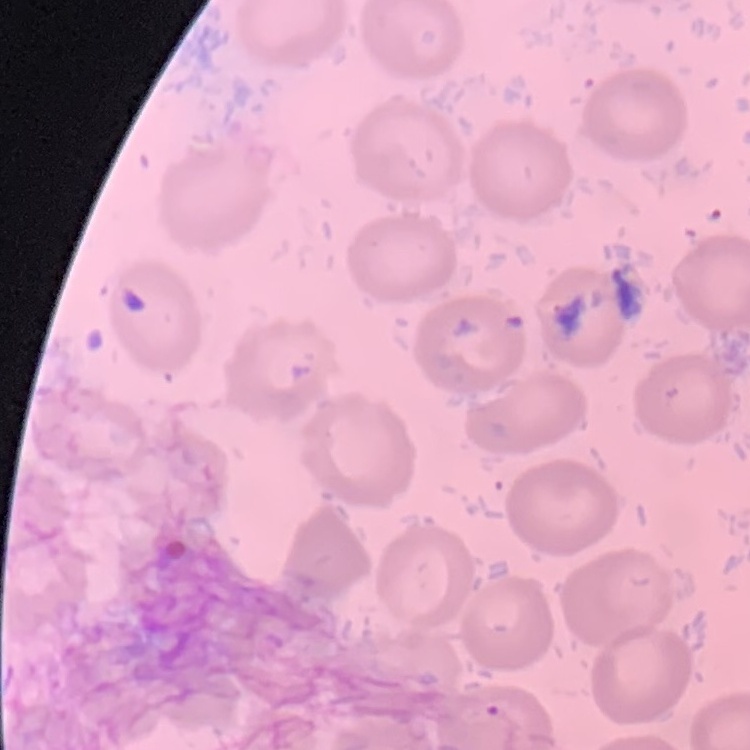
Summary:
  - Erythrocyte morphology: no rouleaux formation
  - Image type: square crop of a larger photomicrograph
  - Stain: Field's or Giemsa
  - Preparation: thin blood film